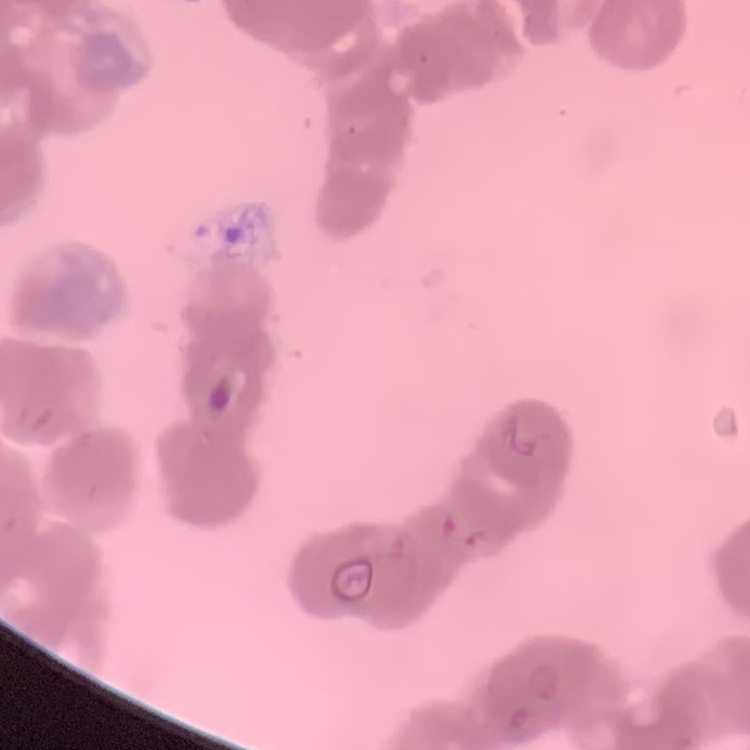

red_blood_cell_morphology: rouleaux formation
stain: Field's or Giemsa
image_type: one tile cut from a larger photomicrograph
preparation: thin blood smear